Draw a bounding box around every leukocyte (white blood cell).
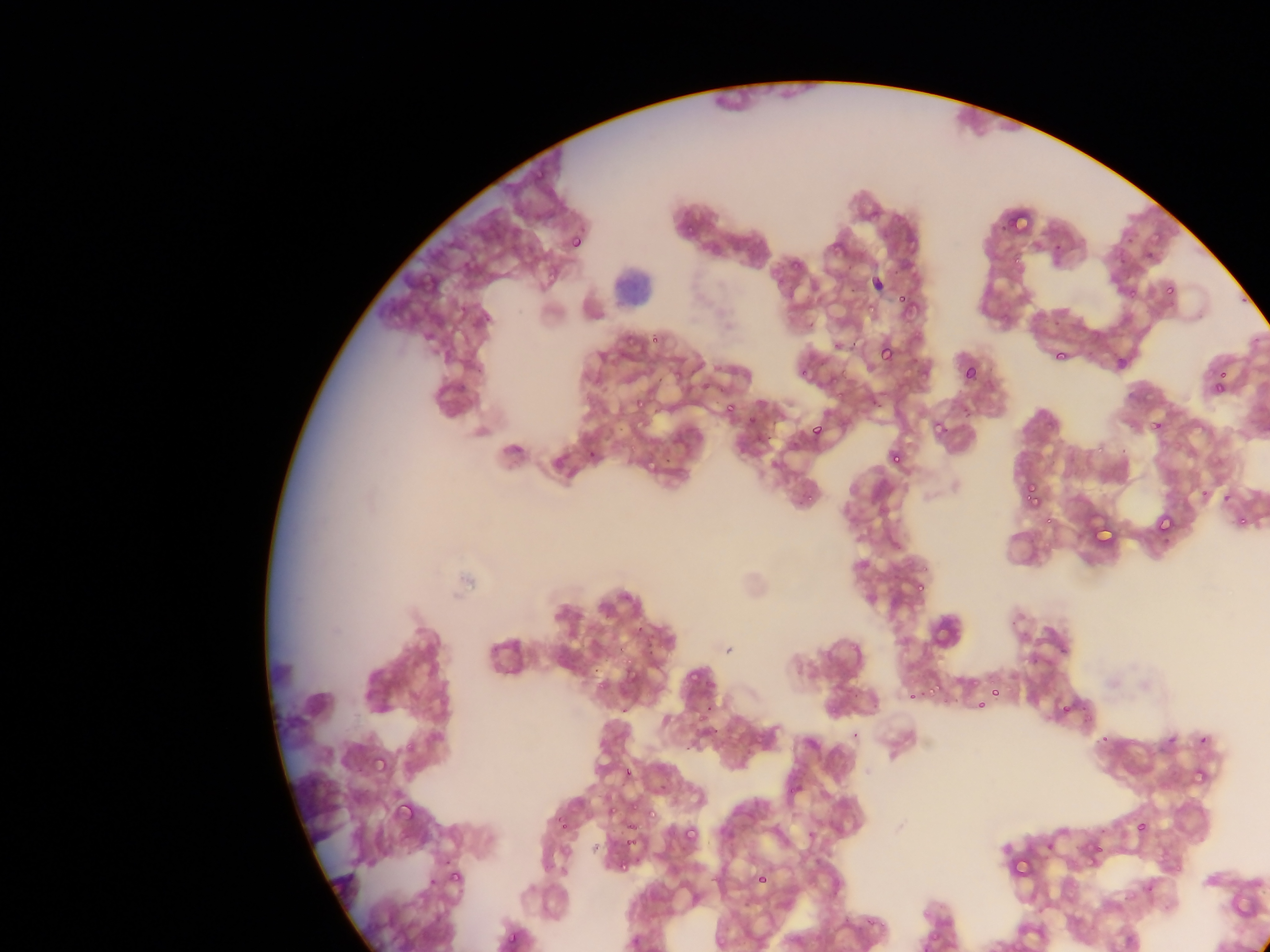
No leukocytes observed.

Approximate bounding boxes as left top right bottom in pixels.
Summary:
  - Plasmodium parasite locations: 1010 208 1038 235; 682 225 702 240; 565 226 593 259; 824 241 850 258; 790 253 810 271; 1126 284 1143 300; 895 288 917 304; 1158 288 1172 298; 866 302 878 315; 621 327 643 346; 651 332 664 344; 1046 339 1067 363; 876 342 897 366; 795 359 819 385; 960 363 980 386; 1209 373 1232 402; 635 384 648 412; 721 398 740 420; 927 410 952 437; 745 412 761 430; 1145 414 1169 437; 809 419 829 443; 886 446 907 469; 641 454 661 471; 1020 482 1045 511; 1154 511 1179 540; 1041 516 1053 528; 1237 517 1257 532; 1091 526 1122 551; 911 576 930 597; 684 658 708 681; 621 661 643 687; 926 668 950 696; 904 678 927 703; 987 686 1002 702; 972 694 986 711; 701 699 719 721; 1056 699 1075 721; 400 737 419 761; 372 754 393 778; 619 763 638 782; 1190 764 1218 790; 393 797 419 826; 607 799 622 814; 644 809 658 819; 554 812 573 832; 623 820 644 846; 1127 822 1153 837; 681 824 701 847; 1086 830 1121 865; 1018 835 1038 874; 618 853 637 875; 448 860 472 881; 759 868 775 888; 505 929 523 948
  - Capture: mobile-phone photograph through a microscope
  - Image size: 1270×952 pixels
  - Preparation: thin blood film
  - Field of view: single
  - Country: Ghana